Locate every malaria parasite.
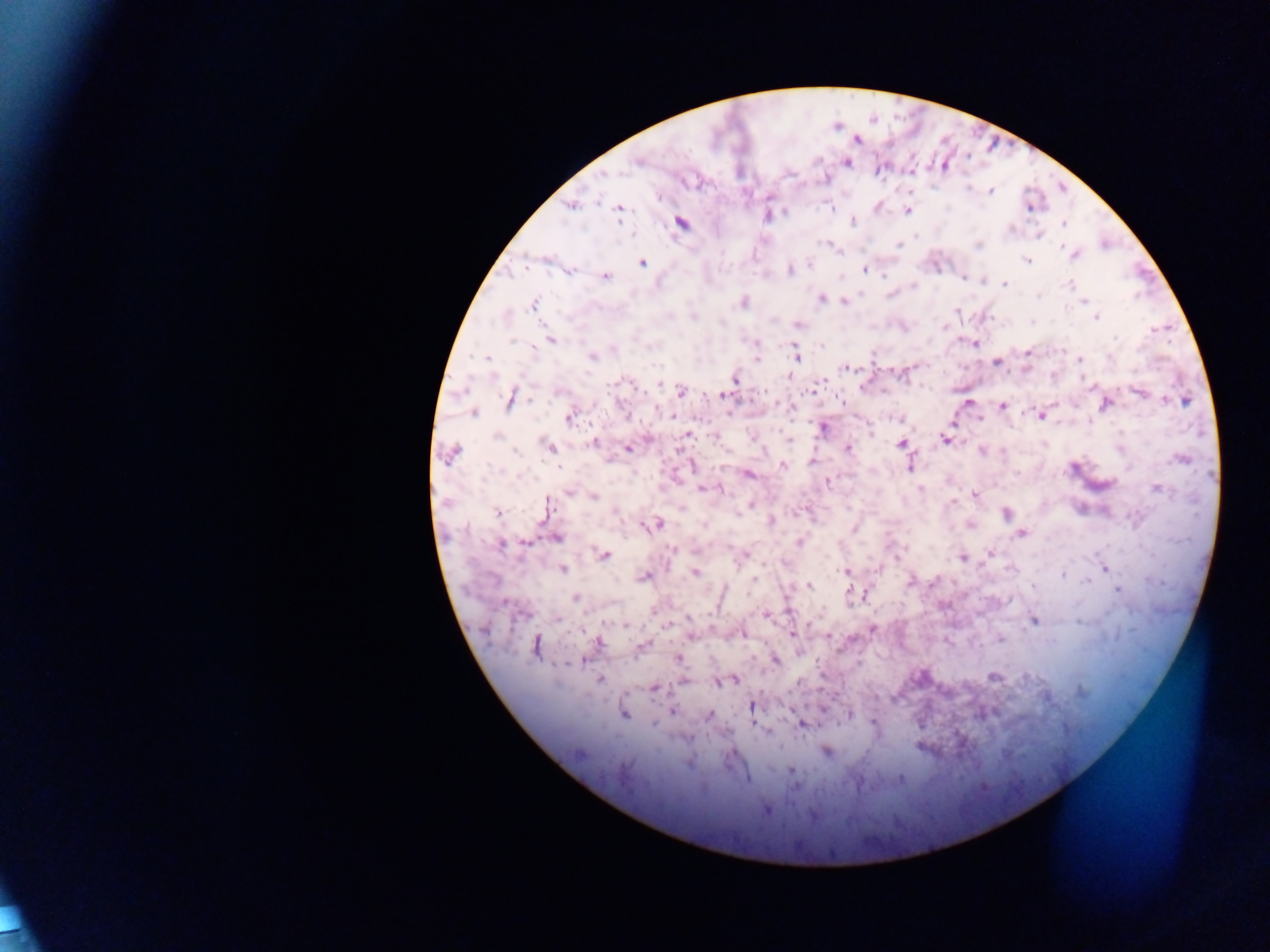

Approximate centers as (x, y) in pixels.
Malaria parasites: (856, 140), (638, 160), (846, 163), (602, 175), (990, 191), (570, 206), (831, 208), (1029, 208), (909, 209), (618, 210), (784, 212), (766, 216), (852, 222), (681, 223), (1063, 224), (828, 244), (898, 245), (978, 245), (1062, 249), (1075, 255), (1027, 260), (642, 262), (809, 264), (790, 269), (864, 269), (570, 271), (605, 276), (884, 276), (963, 278), (1004, 284), (1068, 284), (913, 285), (890, 295), (1038, 296), (821, 299), (744, 302), (845, 302), (1084, 302), (533, 304), (957, 310), (694, 318), (1095, 318), (797, 325), (945, 327), (1115, 338), (550, 340), (512, 341), (973, 343), (756, 344), (822, 345), (1061, 350), (1028, 352), (796, 355), (592, 357), (487, 358), (1109, 358), (756, 359), (1079, 359), (996, 363), (846, 367), (788, 377), (735, 380), (628, 382), (661, 384), (680, 392), (1138, 392), (722, 395), (510, 400), (531, 400), (1165, 400), (842, 402), (1186, 402), (968, 403), (1105, 405), (1002, 406), (789, 407), (473, 413), (626, 416), (671, 416), (1041, 416), (569, 418), (979, 419), (822, 429), (870, 432), (687, 434), (496, 436), (945, 439), (593, 443), (901, 443), (550, 447), (627, 448), (848, 448), (981, 451), (515, 452), (451, 454), (1181, 459), (812, 462), (783, 466), (909, 467), (749, 474), (827, 483), (1156, 488), (702, 489), (920, 489), (720, 490), (568, 494), (975, 494), (593, 497), (952, 503), (750, 505), (547, 507), (682, 508), (498, 513), (1005, 514), (771, 521), (658, 523), (704, 525), (970, 525), (650, 526), (854, 529), (1021, 534), (557, 538), (525, 542), (800, 542), (501, 545), (672, 549), (896, 553), (989, 553), (604, 555), (743, 556), (962, 558), (1105, 568), (876, 569), (562, 570), (696, 572), (846, 572), (1063, 575), (643, 577), (754, 579), (910, 581), (934, 581), (1087, 581), (808, 585), (1118, 590), (848, 591), (853, 593), (864, 594), (575, 598), (653, 613), (766, 615), (689, 618), (558, 619), (1035, 621), (626, 626), (667, 626), (873, 630), (743, 634), (791, 634), (690, 636), (829, 637), (1000, 639), (598, 643), (535, 646), (677, 659), (775, 660), (580, 661), (569, 664), (993, 677), (600, 680), (735, 680), (684, 681), (722, 681), (718, 684), (654, 688), (1080, 691), (751, 707), (823, 708), (672, 712), (623, 714), (708, 714), (849, 714), (873, 723), (802, 724), (654, 725), (765, 732), (826, 752), (688, 763), (791, 770), (901, 778), (795, 787), (766, 811).

capture: mobile-phone photograph through a microscope
country: Ghana
image_size: 1270×952 pixels
field_of_view: single
preparation: thick blood film